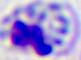
Summary:
  - Identification: white blood cell
  - Magnification: 400x
  - Modality: micrograph